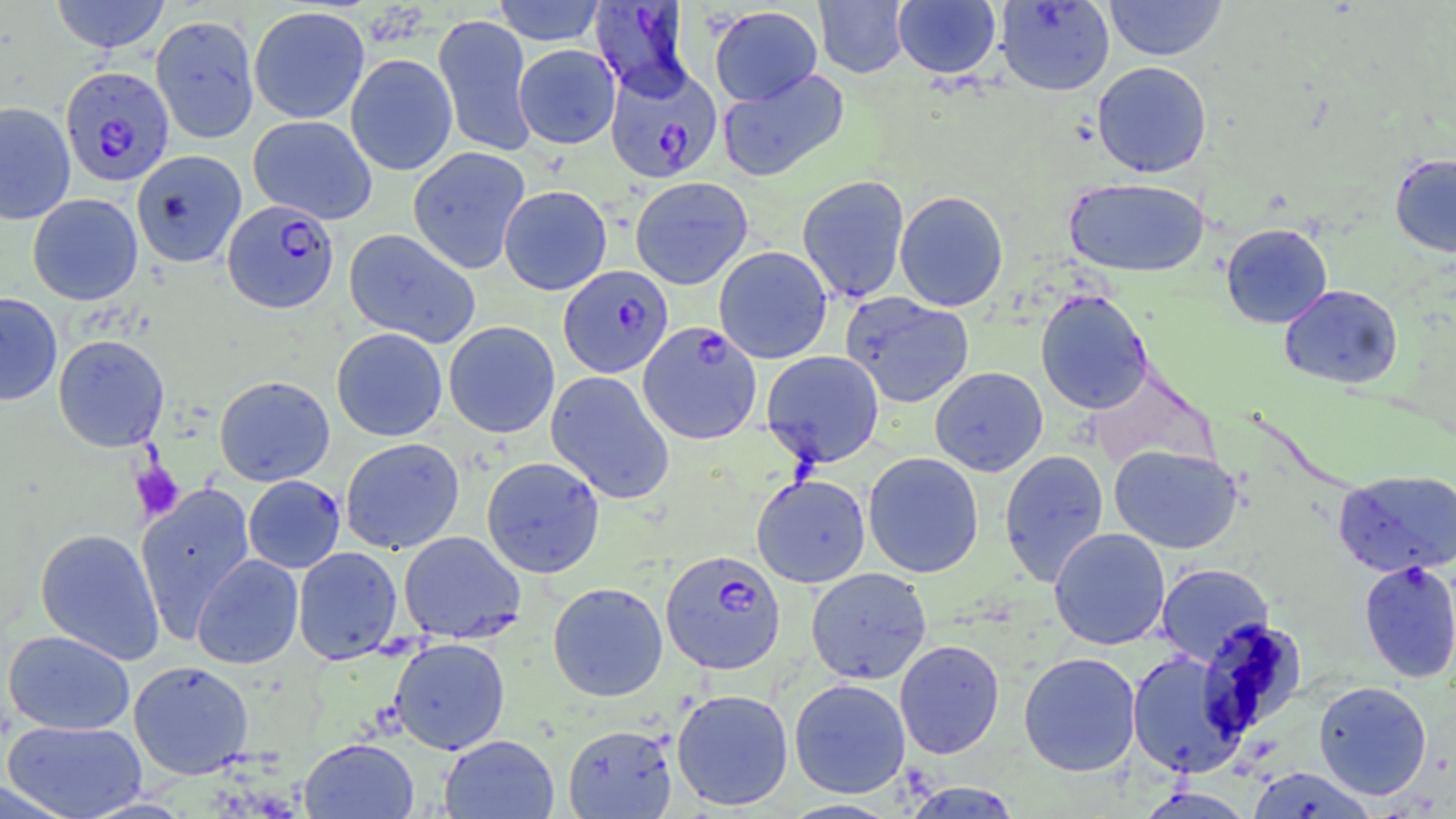

slide-level diagnosis = Plasmodium falciparum
field of view = one of a larger specimen
Plasmodium falciparum-infected red blood cell locations = approximate bounding boxes as (x1, y1, x2, y2) in pixels: (592, 3, 699, 115), (605, 64, 722, 182), (60, 65, 174, 187), (222, 199, 340, 313), (558, 265, 673, 378), (637, 321, 762, 445), (660, 550, 785, 674)
platelet locations = approximate bounding boxes as (x1, y1, x2, y2) in pixels: (130, 461, 184, 522)
magnification = 1000x
uninfected red blood cell locations = approximate bounding boxes as (x1, y1, x2, y2) in pixels: (50, 0, 170, 53), (492, 0, 607, 45), (814, 0, 909, 78), (892, 0, 1001, 78), (1103, 0, 1227, 61), (995, 1, 1115, 95), (248, 5, 370, 124), (709, 5, 822, 106), (150, 14, 260, 143), (433, 14, 535, 157), (514, 44, 621, 149), (346, 53, 457, 175), (1091, 61, 1212, 177), (718, 69, 849, 182), (0, 102, 75, 225), (249, 115, 377, 224), (407, 146, 530, 274), (131, 149, 246, 267), (1389, 153, 1456, 257), (797, 175, 910, 303), (630, 176, 753, 290), (1065, 178, 1210, 276), (499, 185, 612, 295), (894, 190, 1009, 311), (28, 193, 143, 305), (1221, 223, 1333, 328), (344, 228, 481, 348), (714, 246, 832, 363), (1279, 284, 1403, 389), (1035, 289, 1153, 414), (841, 291, 974, 408), (0, 292, 63, 406), (444, 321, 559, 438), (331, 327, 448, 441), (53, 334, 169, 452), (761, 350, 884, 468), (930, 366, 1048, 476), (546, 371, 675, 504), (214, 375, 335, 486), (340, 437, 464, 554), (1109, 445, 1243, 554), (999, 449, 1110, 587), (863, 452, 984, 578), (481, 456, 605, 578), (1334, 468, 1456, 577), (751, 473, 871, 588), (243, 475, 345, 573), (135, 481, 256, 643), (35, 527, 165, 665), (1048, 527, 1170, 650), (398, 530, 526, 643), (293, 546, 403, 664), (192, 554, 303, 669), (1358, 560, 1456, 684), (1156, 562, 1274, 665), (806, 567, 932, 684), (548, 582, 668, 701), (1198, 619, 1308, 738), (3, 629, 135, 735), (389, 637, 510, 754), (895, 639, 1005, 759), (1127, 650, 1248, 777), (1018, 651, 1142, 777), (128, 660, 254, 779), (789, 678, 911, 798), (1313, 680, 1432, 800), (671, 688, 794, 811), (3, 720, 148, 819), (563, 724, 677, 818), (439, 734, 559, 818), (299, 737, 419, 819), (1247, 767, 1378, 818), (900, 781, 1024, 818), (781, 798, 901, 818)
modality = optical microscopy
stain = May-Grünwald-Giemsa
preparation = thin blood smear
image size = 1456×819 pixels